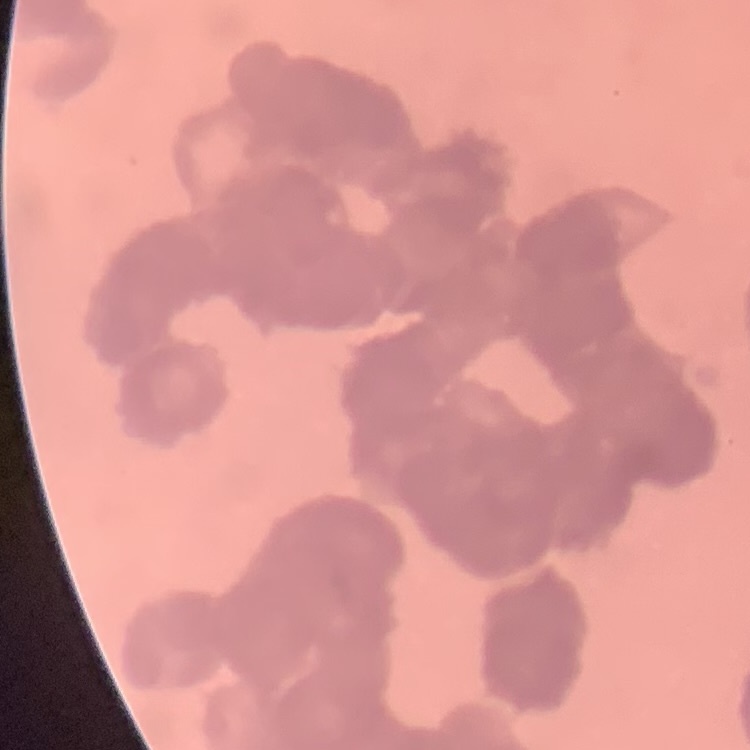
red blood cell morphology = rouleaux formation
image type = one tile cut from a larger photomicrograph
stain = Field's or Giemsa
preparation = thin blood film